Give the position of every Plasmodium parasite visible.
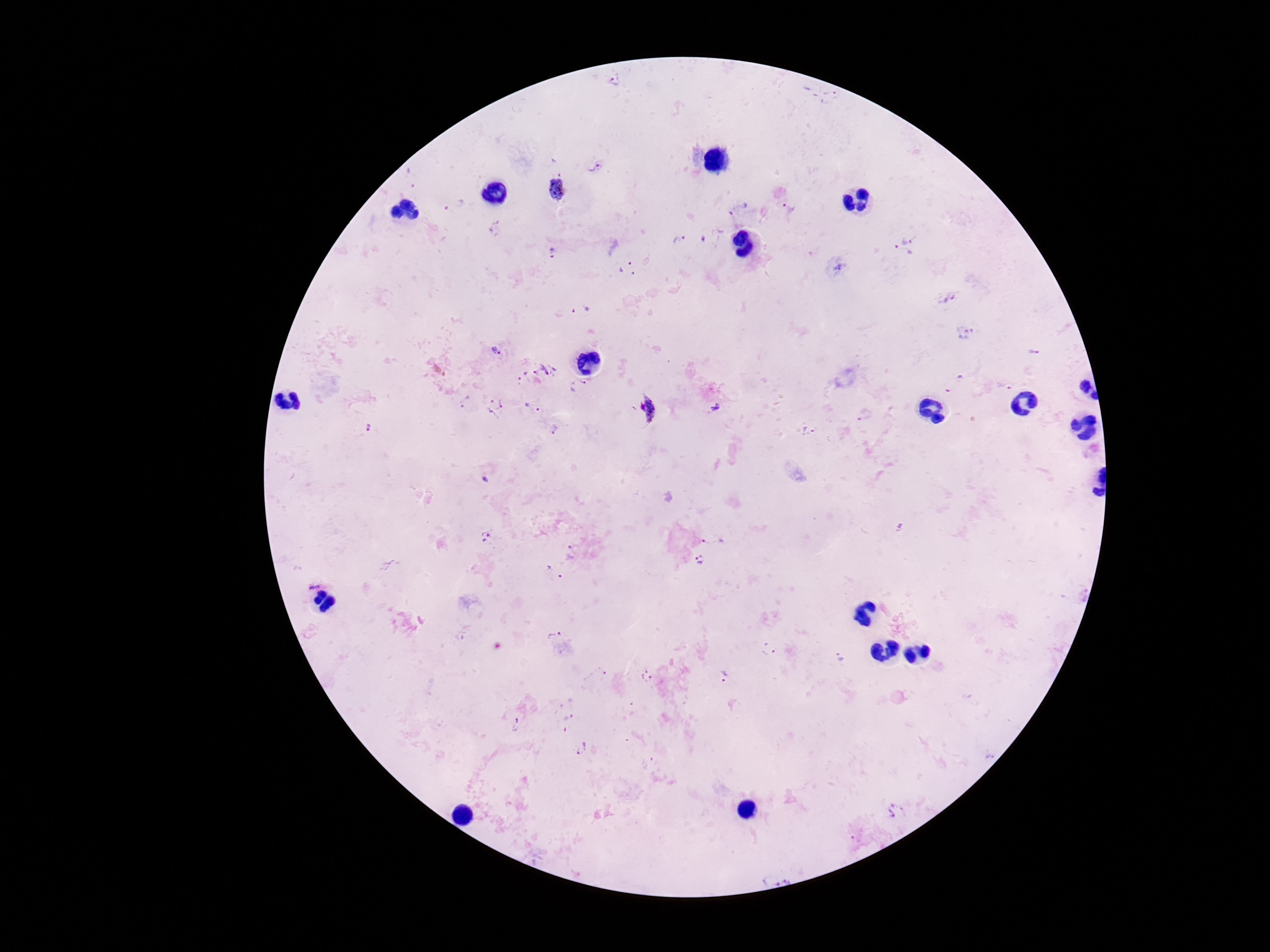
Approximate centers as [x, y] in pixels.
Plasmodium parasites: [615, 81], [837, 94], [596, 167], [556, 189], [455, 203], [737, 207], [787, 209], [498, 231], [906, 235], [680, 241], [901, 253], [554, 254], [625, 267], [837, 268], [950, 298], [582, 310], [965, 334], [496, 351], [1033, 352], [549, 369], [535, 373], [522, 377], [955, 383], [578, 385], [1004, 385], [463, 402], [533, 406], [494, 407], [715, 408], [646, 410], [866, 414], [555, 428], [368, 429], [808, 430], [712, 536], [487, 537], [572, 554], [699, 561], [555, 573], [313, 582], [556, 636], [769, 650], [841, 657], [647, 677], [724, 677], [517, 724], [582, 748], [896, 811], [789, 878], [770, 879].

Giemsa-stained preparation. Patient malaria status: infected. Single field of view. Thick peripheral-blood smear. Photographed through the microscope eyepiece with a smartphone camera. Image is 1270×952 pixels. 100x magnification.